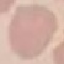

Result: no malaria parasites seen. Thin blood film. Photographed with a smartphone camera at the microscope eyepiece. Giemsa-stained preparation. Automatically extracted cell patch, resized to 64 × 64 pixels.